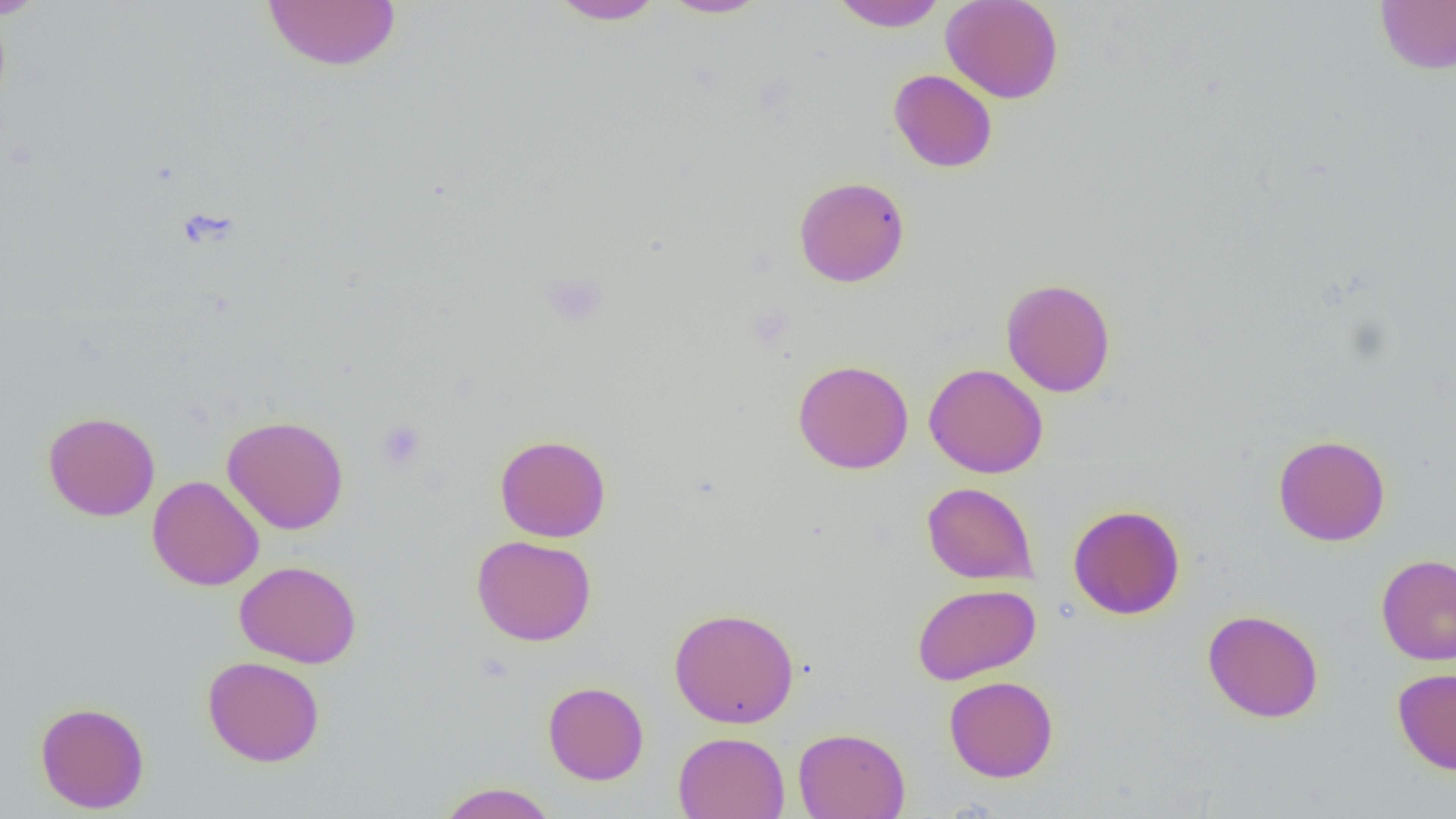
Summary:
  - Coordinate format: approximate bounding boxes as (x1, y1, x2, y2) in pixels
  - Uninfected red blood cell locations: (0, 0, 53, 21), (262, 0, 402, 73), (546, 0, 668, 25), (659, 0, 770, 19), (829, 0, 948, 31), (940, 0, 1064, 104), (1375, 1, 1456, 74), (888, 69, 998, 173), (794, 176, 909, 287), (1001, 278, 1116, 397), (793, 358, 913, 474), (924, 363, 1048, 478), (42, 411, 160, 521), (222, 415, 349, 534), (495, 434, 611, 542), (1273, 434, 1391, 546), (148, 475, 264, 591), (922, 482, 1038, 584), (1068, 504, 1186, 620), (471, 535, 597, 646), (1376, 554, 1456, 665), (234, 560, 362, 668), (912, 583, 1042, 685), (669, 607, 800, 728), (1202, 609, 1324, 723), (202, 655, 325, 767), (1393, 667, 1456, 775), (943, 675, 1059, 783), (543, 681, 649, 785), (35, 701, 150, 814), (793, 727, 910, 819), (673, 731, 790, 819), (435, 782, 560, 819)
  - Platelet locations: (539, 271, 609, 328), (375, 418, 427, 471)
  - Slide-level diagnosis: no evidence of blood parasites
  - Image size: 1456×819 pixels
  - Preparation: thin blood film
  - Modality: optical microscopy
  - Magnification: 1000x
  - Field of view: single